Locate platelets.
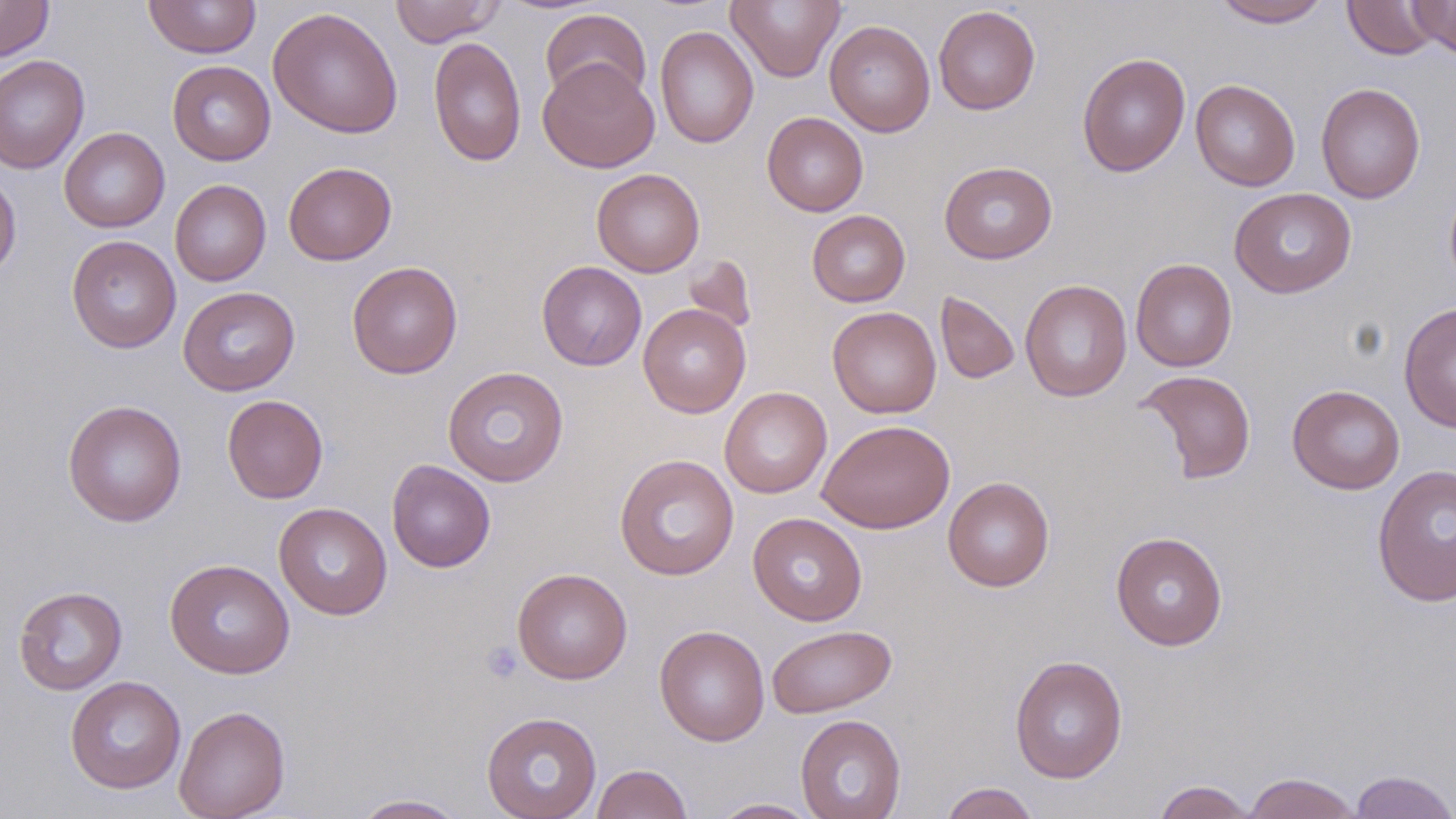
Approximate bounding boxes as (x1, y1, x2, y2) in pixels.
Platelets: (480, 641, 523, 684).

Summary:
  - Uninfected red blood cell locations: (0, 0, 54, 63), (390, 0, 505, 47), (726, 0, 845, 82), (1213, 0, 1331, 28), (1342, 0, 1442, 60), (1408, 0, 1456, 60), (143, 1, 261, 58), (933, 5, 1040, 114), (267, 7, 403, 138), (540, 8, 652, 106), (824, 19, 936, 137), (655, 25, 758, 149), (428, 36, 527, 167), (1077, 52, 1191, 177), (0, 54, 90, 174), (538, 58, 659, 172), (167, 60, 276, 166), (1190, 79, 1300, 191), (1315, 82, 1426, 204), (762, 112, 868, 216), (58, 127, 170, 233), (939, 160, 1057, 264), (283, 161, 396, 265), (592, 168, 705, 277), (0, 172, 21, 282), (1443, 177, 1456, 294), (170, 179, 271, 286), (1229, 187, 1356, 298), (806, 210, 910, 307), (66, 235, 181, 353), (682, 257, 758, 336), (1130, 258, 1237, 372), (347, 261, 463, 379), (536, 261, 647, 371), (1020, 279, 1132, 402), (178, 286, 300, 396), (935, 291, 1020, 384), (1399, 302, 1456, 432), (638, 304, 751, 418), (827, 306, 941, 418), (441, 366, 569, 488), (1136, 369, 1257, 484), (1287, 384, 1405, 494), (720, 387, 832, 498), (222, 395, 328, 503), (62, 399, 187, 527), (817, 419, 955, 533), (614, 454, 739, 581), (386, 459, 495, 572), (1372, 464, 1456, 607), (942, 476, 1055, 592), (273, 502, 392, 620), (749, 512, 867, 626), (1111, 531, 1228, 650), (164, 559, 295, 679), (512, 568, 632, 684), (13, 585, 128, 695), (654, 624, 770, 746), (767, 624, 897, 718), (1009, 655, 1128, 784), (65, 676, 186, 794), (174, 704, 291, 819), (481, 711, 602, 819), (796, 714, 906, 819), (590, 763, 693, 819), (1348, 770, 1456, 819), (1241, 772, 1364, 819), (1152, 780, 1258, 818), (939, 782, 1040, 819), (349, 794, 470, 818), (708, 798, 823, 818)
  - Slide-level diagnosis: no evidence of blood parasites
  - Modality: optical microscopy
  - Image size: 1456×819 pixels
  - Magnification: 1000x
  - Preparation: thin blood film
  - Stain: May-Grünwald-Giemsa
  - Field of view: single